Describe the morphology of the erythrocytes.
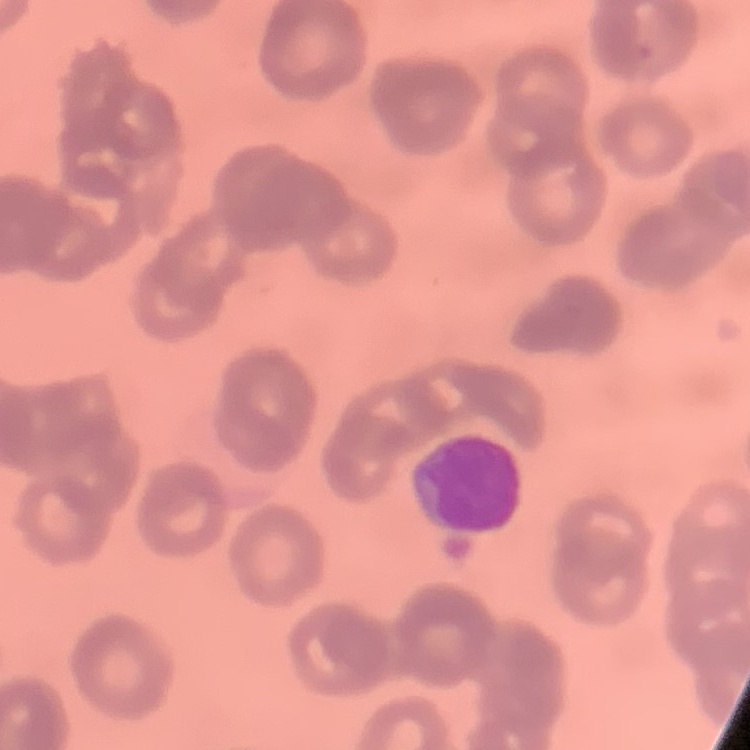
Rouleaux formation.

One tile cut from a larger photomicrograph. Thin peripheral smear. Field's or Giemsa stain.